Point out every Plasmodium parasite.
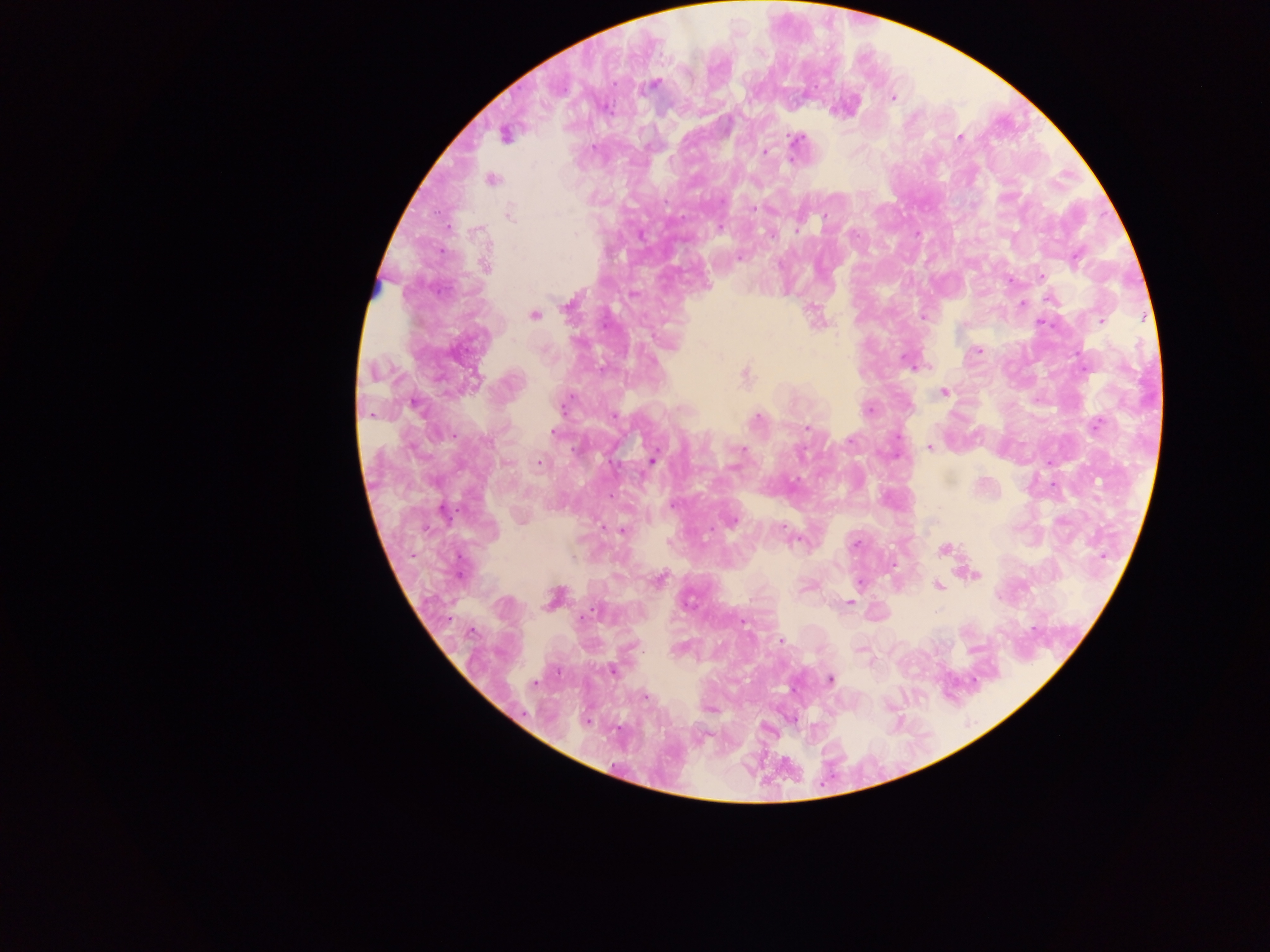
Approximate centers as x y in pixels.
Plasmodium parasites: 655 84; 893 98; 608 109; 504 135; 959 137; 796 140; 764 152; 492 179; 753 209; 509 214; 824 217; 720 227; 797 229; 575 235; 770 235; 1077 257; 739 258; 485 265; 1042 276; 1010 280; 633 294; 1049 299; 1022 304; 534 315; 923 316; 1101 321; 1043 324; 979 351; 904 359; 926 366; 745 374; 944 392; 414 405; 564 405; 869 410; 370 414; 614 416; 757 419; 1096 424; 806 429; 553 432; 850 440; 486 441; 929 446; 743 450; 653 460; 539 463; 734 468; 732 520; 782 527; 621 531; 855 544; 944 549; 1103 556; 975 575; 660 579; 858 583; 939 587; 553 599; 849 603; 590 613; 745 622; 779 641; 861 650; 612 671; 830 680; 534 683; 645 697.

Single field of view. Photographed through a microscope with a mobile-phone camera. Collected in Ghana. Thick blood smear. Image is 1270×952 pixels.